Assess the morphology of the erythrocytes.
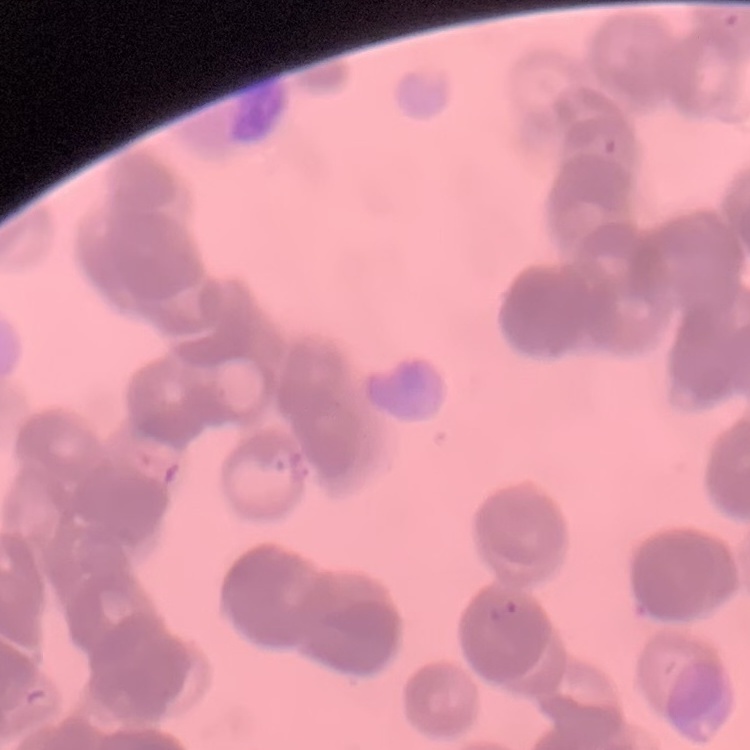

Rouleaux formation.

Thin blood smear. Stained with either Field's or Giemsa. One tile cut from a larger photomicrograph.